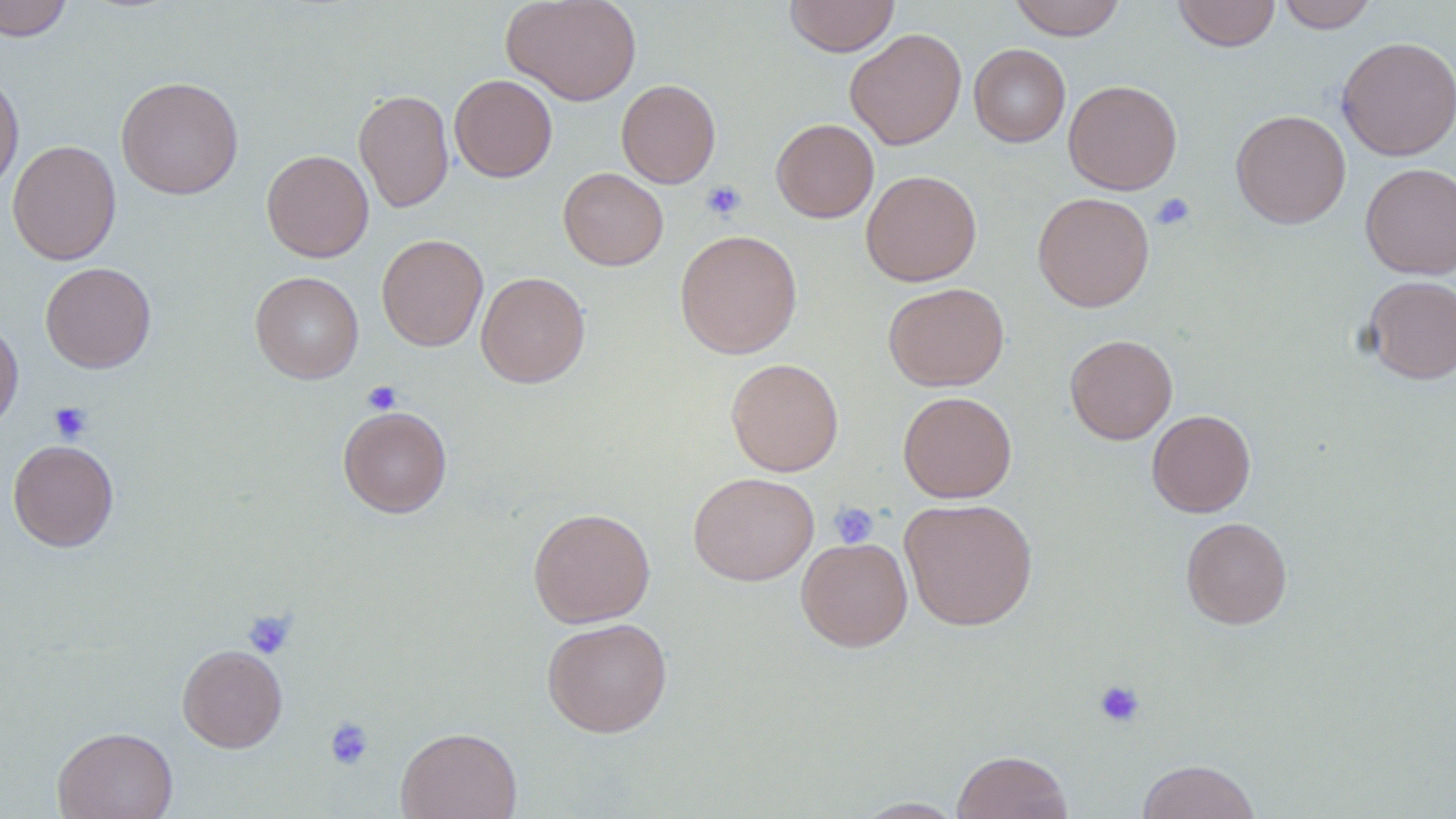

slide-level diagnosis = no evidence of blood parasites
field of view = one of a larger specimen
magnification = 1000x
uninfected red blood cell locations = approximate bounding boxes as [x1, y1, x2, y2] in pixels: [0, 0, 73, 41], [501, 0, 641, 106], [784, 0, 900, 57], [1009, 0, 1126, 41], [1172, 0, 1281, 52], [1276, 0, 1379, 32], [844, 28, 967, 150], [1337, 36, 1456, 161], [969, 43, 1071, 146], [0, 72, 24, 194], [449, 74, 557, 182], [116, 76, 244, 200], [616, 79, 721, 188], [1063, 79, 1182, 195], [353, 88, 454, 213], [1230, 109, 1351, 229], [771, 118, 879, 222], [7, 140, 121, 265], [261, 150, 374, 262], [1360, 162, 1456, 279], [558, 168, 668, 270], [861, 169, 982, 287], [1032, 191, 1154, 311], [675, 229, 803, 359], [376, 233, 488, 351], [40, 262, 156, 373], [250, 271, 364, 384], [476, 271, 591, 388], [1361, 275, 1455, 384], [883, 282, 1010, 391], [0, 318, 23, 436], [1065, 334, 1178, 444], [725, 357, 844, 476], [898, 391, 1017, 502], [338, 406, 452, 517], [1146, 409, 1256, 517], [7, 439, 119, 552], [688, 471, 819, 585], [899, 497, 1038, 631], [528, 507, 655, 627], [1181, 516, 1293, 628], [796, 536, 913, 651], [541, 617, 673, 737], [177, 644, 288, 752], [52, 726, 178, 819], [396, 726, 522, 819], [952, 750, 1074, 819], [1136, 759, 1261, 819], [853, 797, 968, 818]
stain = May-Grünwald-Giemsa
modality = optical microscopy
image size = 1456×819 pixels
platelet locations = approximate bounding boxes as [x1, y1, x2, y2] in pixels: [701, 180, 746, 222], [1150, 192, 1196, 231], [362, 381, 402, 414], [49, 402, 92, 443], [829, 501, 879, 548], [242, 610, 296, 660], [1093, 680, 1146, 728], [324, 716, 375, 770]
preparation = thin blood film